Report the malaria status of this cell.
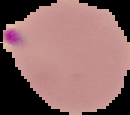
It is parasitized.

Summary:
  - Image size: 130×115 pixels
  - Image type: segmented cell region with the area outside set to black
  - Preparation: thin blood smear